Name the parasite shown.
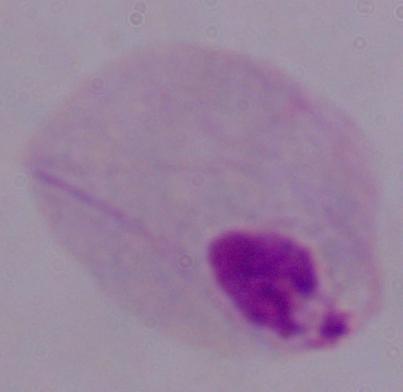

This is a trichomonad.

Summary:
  - Magnification: 1000x
  - Modality: micrograph